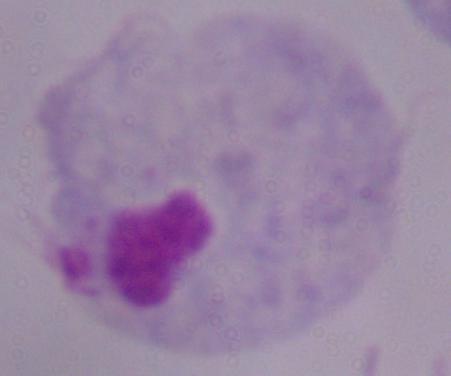
modality = photomicrograph
magnification = 1000x
identification = trichomonad